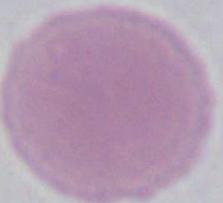 1000x magnification. Photomicrograph. A red blood cell is seen.